Assess this cell for malaria.
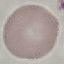
It is uninfected.

Thin blood film. Giemsa-stained preparation. Acquired by smartphone through the microscope eyepiece. Automatically extracted cell patch, resized to 64 × 64 pixels.